Assess this cell for malaria.
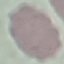

Uninfected.

Thin blood film. Automatically extracted cell patch, resized to 64 × 64 pixels. Photographed with a smartphone camera at the microscope eyepiece. Giemsa-stained preparation.